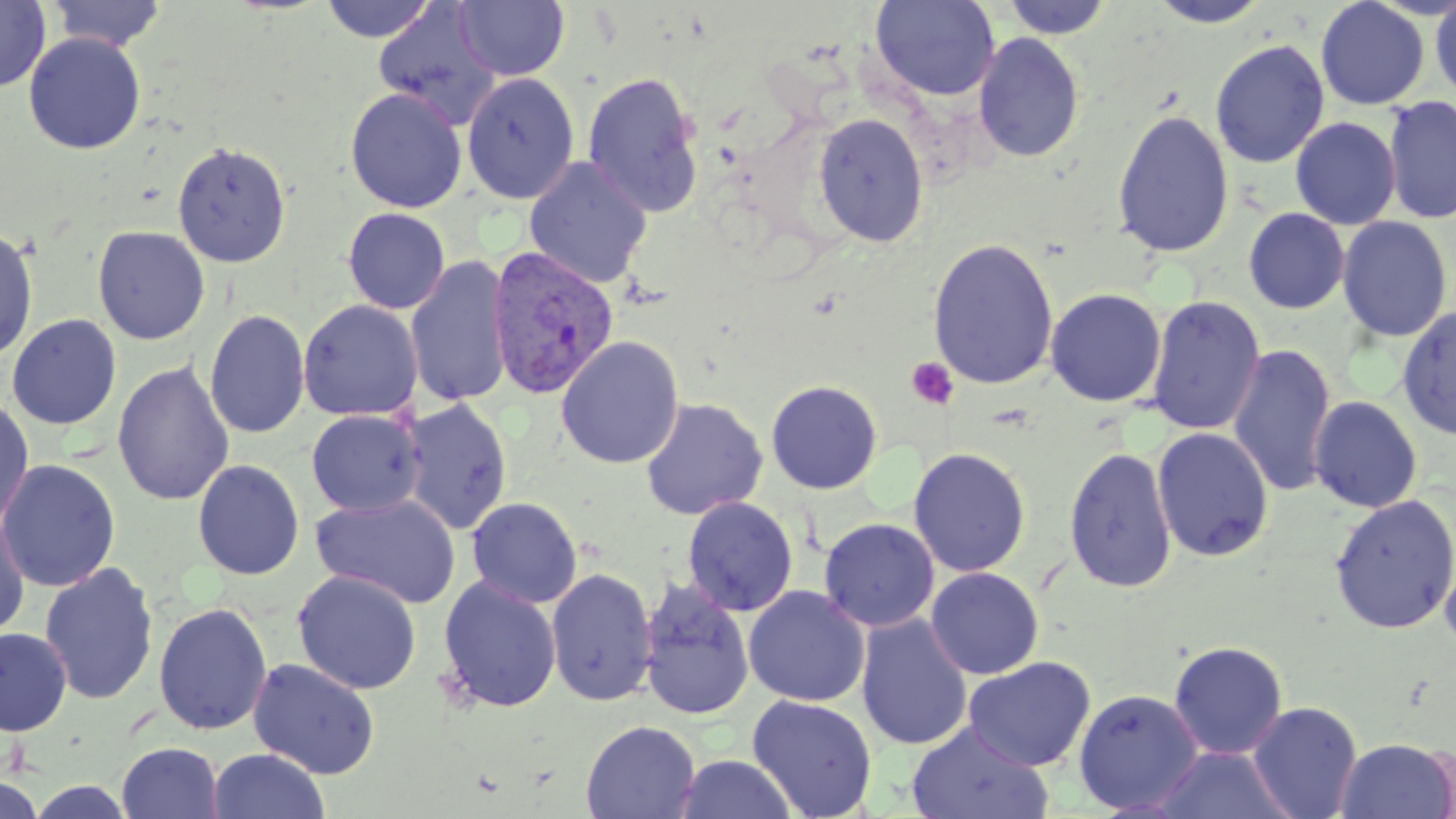

slide-level diagnosis = Plasmodium vivax
field of view = single
Plasmodium vivax-infected red blood cell locations = approximate bounding boxes as (x1,y1)-(x2,y2) corner pairs in pixels: (486,245)-(620,401)
image size = 1456×819 pixels
stain = May-Grünwald-Giemsa
uninfected red blood cell locations = approximate bounding boxes as (x1,y1)-(x2,y2) corner pairs in pixels: (45,0)-(169,52), (318,0)-(439,42), (454,0)-(569,81), (870,0)-(1000,101), (1000,0)-(1114,39), (1315,0)-(1430,110), (1429,0)-(1456,101), (0,1)-(50,92), (1145,1)-(1273,28), (372,4)-(501,128), (23,32)-(146,155), (972,32)-(1085,163), (1209,39)-(1330,169), (582,71)-(705,217), (461,72)-(579,203), (345,88)-(467,213), (1382,94)-(1455,226), (1111,108)-(1234,259), (813,112)-(929,247), (1290,116)-(1401,229), (171,140)-(291,267), (523,156)-(653,290), (342,207)-(450,314), (1243,207)-(1350,314), (1336,215)-(1453,343), (0,225)-(39,363), (92,225)-(210,345), (927,237)-(1059,390), (406,255)-(513,409), (1045,287)-(1167,408), (1146,295)-(1265,436), (298,299)-(422,421), (1396,305)-(1456,441), (204,308)-(310,440), (6,313)-(122,430), (555,335)-(685,469), (1227,342)-(1337,499), (112,360)-(235,506), (766,379)-(882,494), (0,394)-(34,534), (1308,395)-(1423,513), (639,397)-(768,520), (401,398)-(513,536), (306,409)-(425,516), (1152,426)-(1275,562), (1063,445)-(1178,594), (908,447)-(1031,578), (0,458)-(121,593), (192,459)-(305,580), (312,493)-(461,608), (1328,494)-(1456,634), (466,497)-(583,608), (682,497)-(799,617), (0,510)-(31,639), (818,517)-(940,631), (1439,544)-(1456,655), (39,561)-(159,705), (546,567)-(658,706), (925,567)-(1044,680), (293,569)-(422,695), (437,575)-(562,714), (638,579)-(756,721), (743,586)-(870,707), (153,602)-(273,735), (856,613)-(973,751), (1,626)-(72,736), (1168,640)-(1288,760), (964,657)-(1095,772), (247,658)-(380,779), (1072,687)-(1204,814), (746,694)-(878,819), (1247,701)-(1363,819), (580,719)-(701,819), (907,721)-(1052,819), (1334,737)-(1456,819), (116,741)-(223,818), (1152,745)-(1294,819), (208,748)-(330,819), (673,753)-(799,818), (0,774)-(46,819), (25,779)-(136,818)
preparation = thin blood smear
magnification = 1000x
platelet locations = approximate bounding boxes as (x1,y1)-(x2,y2) corner pairs in pixels: (906,357)-(959,410)
modality = light microscopy